Which red blood cells are Plasmodium falciparum-infected, and which are of indeterminate infection status?
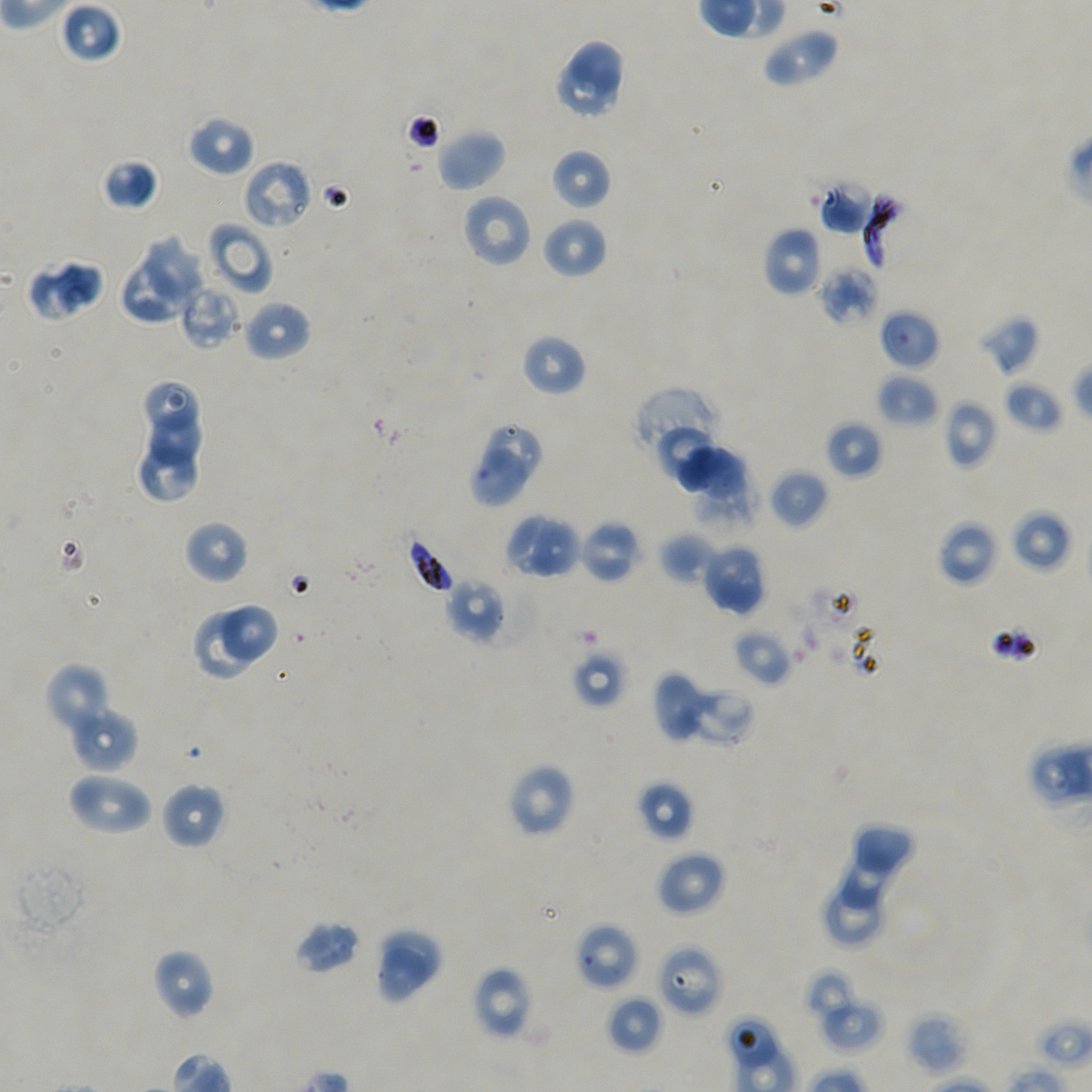
Approximate bounding boxes as [x1, y1, x2, y2] in pixels. Not every red blood cell is marked.
Infected red blood cells: [862, 191, 918, 274], [405, 534, 454, 594].
Red blood cells of indeterminate infection status: [242, 160, 312, 230], [179, 280, 243, 350], [878, 308, 940, 370], [486, 425, 542, 484], [469, 447, 530, 509], [575, 922, 639, 990], [657, 944, 723, 1017], [725, 1015, 780, 1072].

locations_of_uninfected_red_blood_cells: '[57, 1, 122, 65], [762, 26, 839, 88], [568, 40, 624, 98], [553, 59, 617, 120], [185, 114, 255, 178], [435, 128, 507, 192], [551, 149, 612, 211], [100, 158, 160, 211], [816, 179, 875, 235], [460, 193, 532, 268], [542, 217, 608, 280], [206, 222, 273, 296], [762, 226, 822, 297], [142, 235, 205, 307], [26, 257, 106, 321], [117, 259, 189, 325], [818, 266, 879, 327], [241, 299, 312, 361], [977, 314, 1040, 376], [521, 333, 587, 397], [876, 373, 939, 427], [142, 378, 198, 433], [1004, 380, 1063, 433], [632, 387, 721, 472], [944, 399, 998, 469], [147, 404, 201, 468], [824, 420, 882, 479], [659, 426, 715, 486], [136, 445, 198, 500], [674, 445, 746, 505], [769, 468, 829, 530], [1009, 508, 1072, 573], [503, 513, 561, 575], [530, 518, 578, 578], [578, 518, 642, 583], [184, 520, 249, 585], [936, 520, 1000, 587], [659, 532, 717, 584], [700, 541, 767, 615], [445, 577, 507, 642], [217, 605, 278, 663], [190, 612, 257, 682], [733, 628, 793, 687], [571, 649, 627, 709], [45, 662, 114, 738], [653, 670, 703, 742], [680, 685, 755, 747], [67, 705, 139, 773], [507, 763, 576, 838], [66, 770, 153, 836], [637, 780, 695, 841], [160, 782, 225, 850], [853, 824, 917, 876], [839, 849, 903, 908], [656, 850, 727, 916], [820, 888, 884, 947], [294, 920, 362, 975], [382, 930, 439, 986], [374, 946, 429, 1006], [152, 948, 217, 1020], [471, 965, 534, 1040], [804, 967, 860, 1021], [606, 995, 663, 1055], [819, 997, 885, 1053], [907, 1011, 968, 1076]'
culture: Plasmodium falciparum strain NF54, static, in vitro
preparation: thin blood smear
field_of_view: one from this slide
objective: 100x, oil immersion, numerical aperture 1.45
stain: Giemsa
image_size: 1092×1092 pixels
donor_blood_group: A+/O+